Comment on the morphology of the erythrocytes.
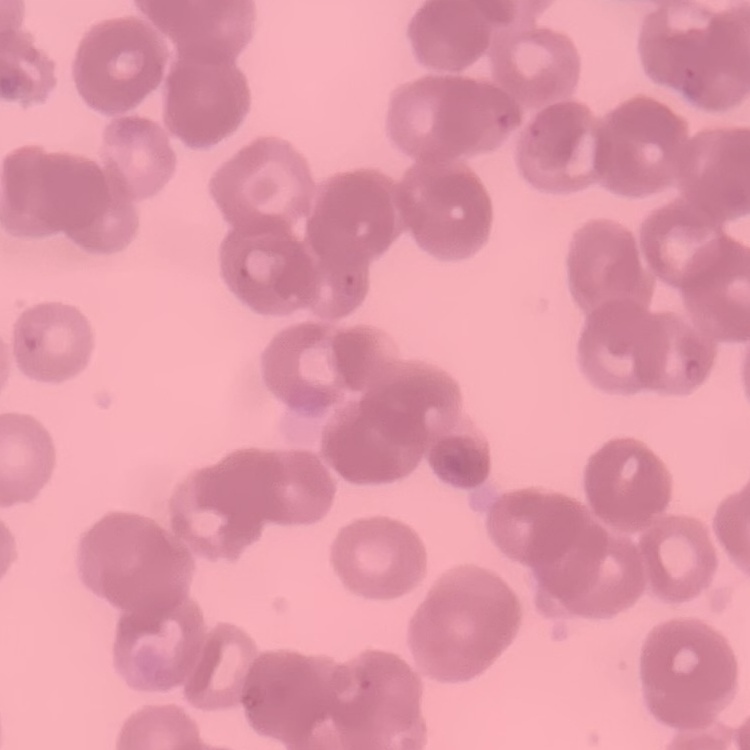
Rouleaux formation.

Stained with either Field's or Giemsa. Thin blood smear. One tile cut from a larger photomicrograph.